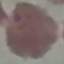
Summary:
  - Result: malaria parasites detected
  - Capture: smartphone camera at the microscope eyepiece
  - Stain: Giemsa
  - Preparation: thin blood smear
  - Image type: cell patch, automatically extracted from a larger field of view and resized to 64 × 64 pixels